Report the malaria status of this cell.
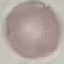
Uninfected.

image type = cell patch, automatically extracted from a larger field of view and resized to 64 × 64 pixels
preparation = thin blood smear
capture = smartphone camera at the microscope eyepiece
stain = Giemsa